Classify this cell by malaria status.
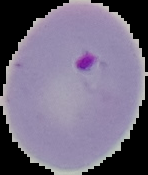
Parasitized.

preparation = thin blood smear
image size = 148×175 pixels
image type = segmented cell region on a black background